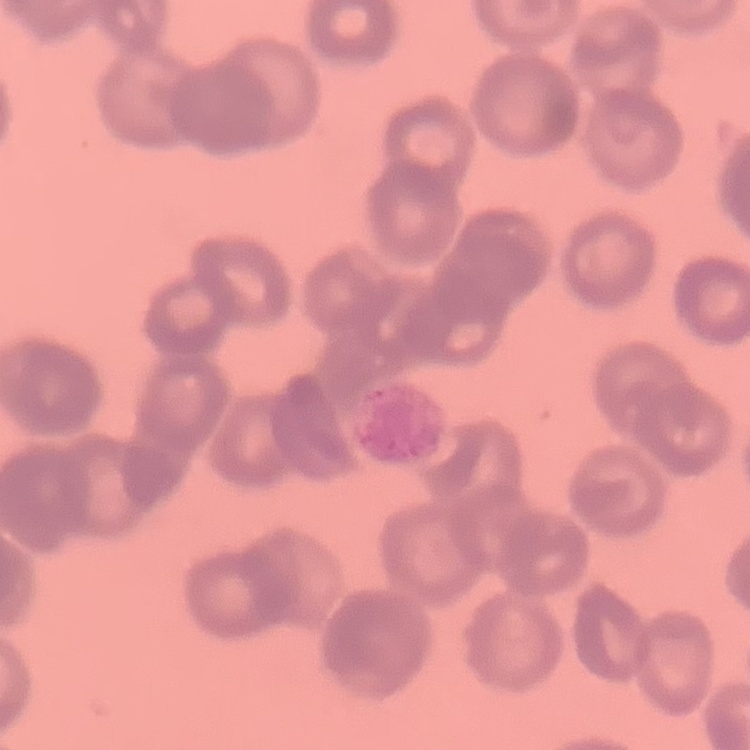

Summary:
  - Erythrocyte morphology: rouleaux formation
  - Image type: one tile cut from a larger photomicrograph
  - Preparation: thin peripheral smear
  - Stain: Field's or Giemsa